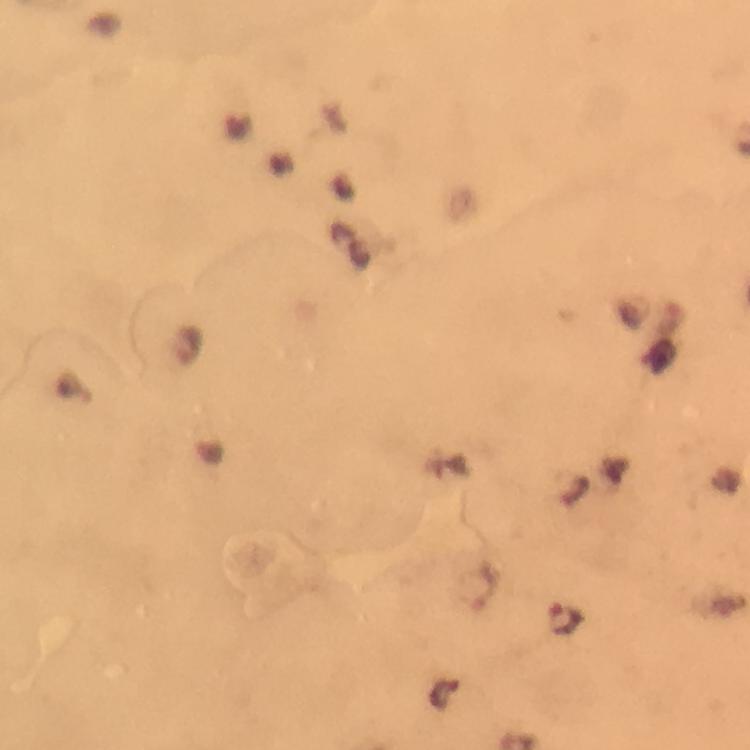
Approximate centers as [x, y] in pixels.
Summary:
  - Plasmodium parasite locations: [188, 345], [77, 389], [564, 620]
  - Cropped from: a single field of view
  - Context: from a malaria diagnostic workup
  - Capture: smartphone photograph through a microscope
  - Magnification: 100x
  - Stain: Giemsa
  - Image size: 750×750 pixels
  - Preparation: thick blood film
  - Immersion oil: used